Name the parasite shown.
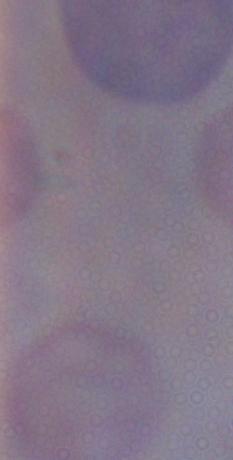
A trypanosome.

Photomicrograph. Captured at 1000x magnification.